Name the parasite shown.
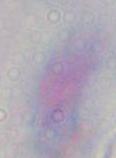
This is Toxoplasma gondii.

Summary:
  - Modality: micrograph
  - Magnification: 1000x